Assess this cell for malaria.
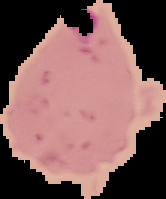

It is parasitized.

The area outside the segmented cell region is set to black. From a thin blood smear. Image is 166×199 pixels.